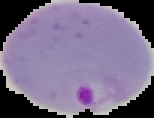

Malaria status: parasitized. The area outside the segmented cell region is set to black. From a thin blood smear. Image is 154×118 pixels.